Give the extent of all Plasmodium falciparum-infected red blood cells.
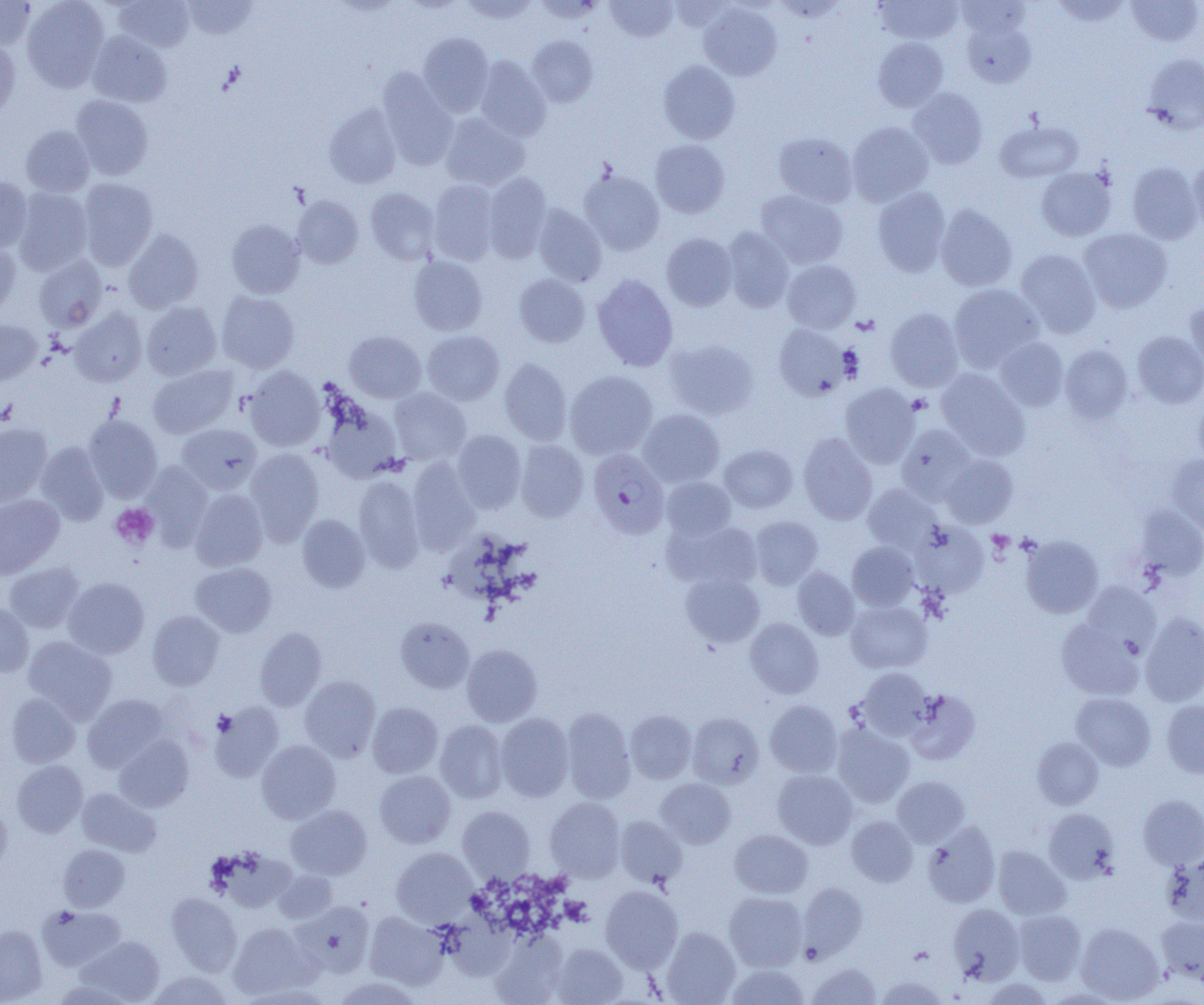
Approximate bounding boxes as (x1, y1, x2, y2) in pixels.
Plasmodium falciparum-infected red blood cells: (589, 447, 671, 538).

Summary:
  - Uninfected red blood cell locations: (0, 0, 35, 50), (22, 0, 109, 91), (115, 0, 194, 52), (459, 0, 539, 24), (605, 0, 678, 41), (875, 0, 963, 44), (1051, 0, 1131, 26), (1126, 0, 1203, 47), (183, 1, 257, 40), (672, 1, 732, 32), (698, 3, 782, 81), (960, 15, 1037, 88), (88, 31, 171, 107), (417, 32, 494, 116), (528, 36, 598, 108), (873, 37, 949, 112), (0, 38, 20, 122), (1142, 52, 1204, 133), (474, 57, 551, 141), (658, 60, 740, 144), (377, 69, 459, 168), (907, 88, 988, 168), (70, 95, 153, 180), (324, 104, 401, 189), (440, 113, 529, 190), (994, 119, 1083, 182), (847, 121, 934, 206), (21, 125, 94, 197), (774, 132, 858, 207), (651, 139, 729, 218), (1188, 156, 1204, 231), (1127, 162, 1202, 244), (1036, 167, 1116, 241), (580, 169, 664, 255), (482, 172, 552, 261), (0, 177, 33, 251), (77, 178, 158, 269), (428, 180, 500, 265), (365, 187, 439, 265), (873, 187, 951, 276), (14, 188, 92, 275), (755, 190, 848, 268), (292, 196, 364, 268), (533, 204, 607, 286), (936, 204, 1017, 291), (226, 219, 305, 298), (722, 227, 794, 312), (1079, 228, 1172, 312), (123, 229, 203, 314), (661, 233, 738, 311), (0, 239, 20, 317), (1016, 249, 1101, 338), (33, 256, 107, 331), (409, 256, 487, 336), (782, 259, 861, 333), (514, 274, 590, 347), (592, 274, 678, 371), (949, 284, 1043, 371), (216, 290, 299, 373), (1184, 300, 1204, 377), (142, 302, 222, 380), (70, 307, 147, 386), (885, 307, 964, 391), (0, 320, 42, 385), (774, 324, 849, 400), (344, 330, 426, 402), (422, 330, 504, 405), (1132, 330, 1204, 408), (995, 337, 1068, 410), (665, 339, 760, 419), (1059, 344, 1133, 423), (499, 358, 572, 445), (148, 364, 238, 438), (244, 366, 325, 451), (936, 368, 1029, 459), (565, 370, 658, 460), (840, 383, 920, 467), (389, 388, 470, 465), (1194, 397, 1204, 468), (320, 399, 403, 483), (638, 409, 725, 487), (83, 415, 162, 501), (0, 423, 52, 506), (177, 423, 261, 494), (896, 424, 976, 504), (452, 429, 526, 513), (798, 433, 878, 525), (515, 439, 589, 521), (36, 442, 109, 525), (719, 444, 798, 513), (245, 448, 325, 543), (942, 455, 1018, 528), (1167, 455, 1204, 536), (407, 459, 480, 555), (141, 464, 213, 547), (353, 476, 424, 573), (661, 477, 735, 541), (864, 484, 940, 553), (190, 489, 268, 571), (0, 494, 63, 578), (1137, 504, 1204, 580), (296, 514, 370, 592), (750, 516, 823, 588), (666, 520, 762, 591), (913, 522, 989, 598), (1021, 535, 1104, 618), (847, 542, 919, 611), (3, 562, 84, 633), (191, 562, 276, 637), (792, 567, 859, 640), (681, 572, 765, 647), (63, 577, 150, 659), (1081, 582, 1161, 655), (846, 600, 932, 673), (0, 601, 34, 677), (147, 611, 223, 690), (1140, 611, 1204, 706), (395, 617, 474, 693), (745, 618, 823, 698), (1056, 618, 1144, 700), (254, 627, 327, 711), (23, 636, 117, 723), (462, 644, 542, 726), (857, 667, 932, 740), (299, 675, 380, 762), (905, 690, 980, 765), (1071, 692, 1156, 770), (6, 693, 80, 768), (83, 694, 170, 773), (765, 700, 842, 778), (1161, 700, 1204, 778), (210, 702, 284, 781), (367, 702, 442, 778), (560, 707, 636, 803), (625, 710, 697, 783), (687, 712, 764, 789), (495, 713, 574, 802), (434, 720, 508, 803), (831, 725, 915, 808), (114, 735, 194, 812), (1032, 737, 1104, 809), (257, 740, 340, 823), (11, 760, 88, 837), (772, 769, 857, 849), (375, 770, 455, 848), (892, 776, 969, 846), (656, 778, 736, 848), (77, 788, 161, 856), (1138, 795, 1204, 869), (545, 797, 625, 881), (0, 802, 12, 876), (287, 805, 371, 879), (457, 806, 535, 880), (1044, 808, 1120, 884), (615, 816, 687, 889), (846, 816, 918, 886), (923, 821, 1000, 907), (729, 829, 813, 899), (57, 844, 129, 911), (993, 845, 1071, 921), (391, 847, 476, 925), (1162, 854, 1204, 927), (273, 869, 338, 924), (797, 881, 868, 960), (601, 886, 683, 972), (166, 892, 242, 975), (725, 892, 807, 971), (445, 899, 524, 974), (293, 901, 374, 976), (948, 903, 1025, 984), (37, 905, 125, 971), (1013, 908, 1086, 985), (365, 911, 448, 990), (1157, 917, 1204, 987), (228, 922, 318, 999), (1076, 922, 1164, 1003), (0, 925, 48, 1004), (661, 927, 740, 1004), (491, 934, 566, 1005), (79, 936, 164, 1003), (551, 943, 627, 1004), (808, 962, 881, 1005), (725, 963, 809, 1005), (147, 971, 235, 1005), (876, 975, 948, 1005), (333, 976, 423, 1005), (981, 977, 1054, 1005)
  - Platelet locations: (907, 393, 931, 414), (110, 503, 159, 549), (987, 530, 1014, 554), (211, 710, 235, 736)
  - Slide-level diagnosis: Plasmodium falciparum
  - Modality: light microscopy
  - Magnification: 1000x
  - Field of view: single
  - Image size: 1204×1005 pixels
  - Preparation: thin blood film